Locate every blood parasite and identify its species.
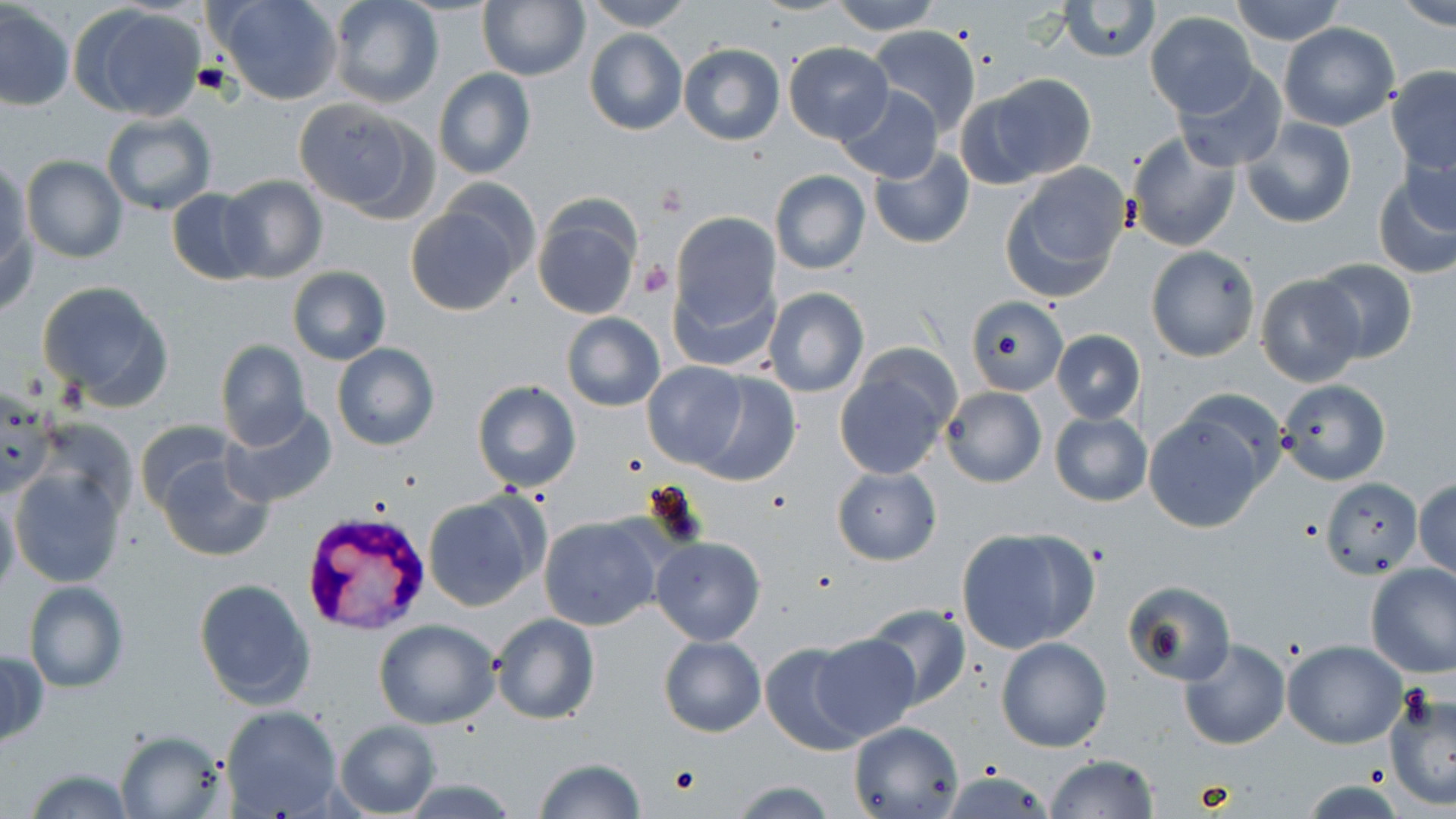

Approximate bounding boxes as (x1,y1)-(x2,y2) corner pairs in pixels.
Plasmodium vivax-infected red blood cells: (302,519)-(429,636).
No Plasmodium falciparum, Plasmodium ovale, Plasmodium malariae, Babesia divergens, or Trypanosoma brucei observed.

slide-level diagnosis = Plasmodium vivax
field of view = single
magnification = 1000x
modality = light microscopy
stain = May-Grünwald-Giemsa
platelet locations = approximate bounding boxes as (x1,y1)-(x2,y2) corner pairs in pixels: (639,259)-(674,297), (671,765)-(702,793)
image size = 1456×819 pixels
uninfected red blood cell locations = approximate bounding boxes as (x1,y1)-(x2,y2) corner pairs in pixels: (215,0)-(342,105), (476,0)-(590,82), (584,0)-(692,31), (828,0)-(941,34), (1056,0)-(1161,64), (1228,0)-(1347,46), (1392,0)-(1455,29), (328,1)-(444,109), (1,4)-(74,111), (70,4)-(207,123), (1145,11)-(1257,118), (1278,22)-(1399,131), (866,26)-(981,133), (584,29)-(686,135), (783,42)-(893,145), (679,44)-(785,146), (1385,66)-(1455,176), (1173,67)-(1287,171), (433,68)-(536,179), (985,74)-(1095,181), (836,86)-(943,183), (293,97)-(434,220), (100,112)-(215,215), (1240,119)-(1357,228), (1125,131)-(1241,251), (867,146)-(975,250), (20,155)-(128,262), (0,162)-(30,278), (1372,162)-(1455,280), (999,163)-(1132,302), (770,170)-(871,276), (215,173)-(329,283), (166,188)-(266,286), (532,199)-(642,322), (406,206)-(522,315), (671,212)-(781,332), (1144,245)-(1260,361), (1309,258)-(1417,364), (287,266)-(391,364), (667,273)-(778,374), (1254,274)-(1368,389), (38,280)-(173,408), (763,287)-(868,397), (963,295)-(1067,396), (562,313)-(665,411), (1052,330)-(1145,423), (215,341)-(311,450), (332,343)-(441,451), (834,357)-(957,478), (641,360)-(747,469), (692,373)-(801,486), (1277,379)-(1391,485), (472,381)-(582,494), (0,385)-(55,500), (940,386)-(1046,488), (1145,405)-(1275,532), (218,406)-(337,508), (1050,411)-(1152,507), (32,417)-(137,520), (134,420)-(238,515), (156,453)-(273,562), (832,467)-(940,564), (10,470)-(126,587), (1322,477)-(1422,577), (1414,477)-(1456,581), (0,489)-(20,602), (423,494)-(542,611), (539,515)-(662,631), (956,528)-(1098,654), (651,538)-(765,645), (1365,562)-(1456,676), (194,579)-(316,710), (24,580)-(129,694), (1125,580)-(1236,686), (860,603)-(972,710), (490,612)-(599,725), (374,619)-(500,729), (658,635)-(765,737), (811,635)-(918,740), (995,638)-(1111,752), (1178,639)-(1289,750), (759,640)-(870,755), (1282,640)-(1406,748), (0,648)-(47,749), (1384,689)-(1456,809), (220,705)-(343,818), (335,719)-(440,819), (847,721)-(963,819), (115,729)-(230,817), (1043,755)-(1160,817), (533,759)-(648,818), (22,766)-(135,819), (941,771)-(1055,817), (400,779)-(522,816), (726,779)-(839,818), (1304,780)-(1403,817)
preparation = thin blood smear